Point out each Plasmodium parasite.
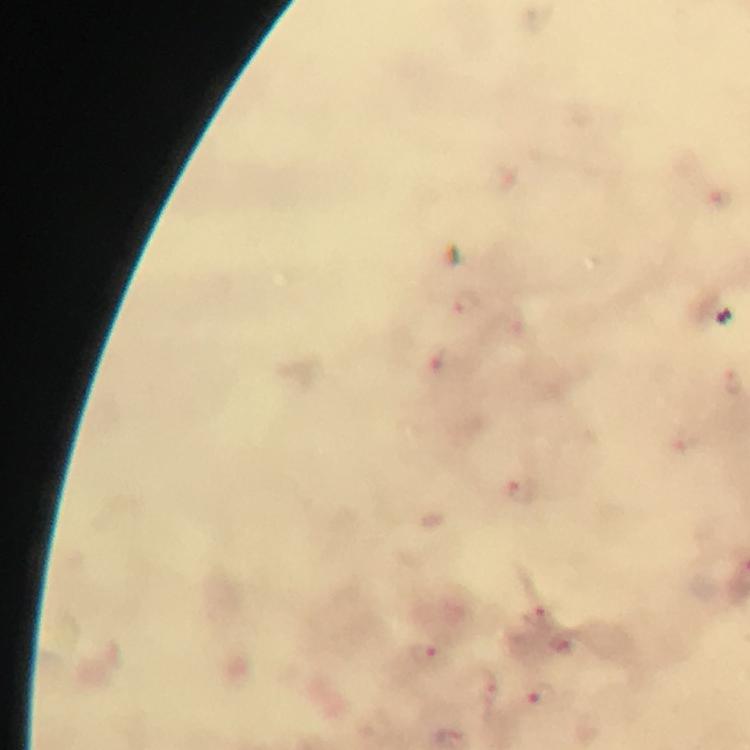
Approximate centers as {x, y} in pixels.
Plasmodium parasites: {721, 200}, {466, 302}, {435, 359}, {734, 383}, {519, 490}, {537, 616}, {564, 643}, {425, 655}, {487, 692}, {543, 694}.

Summary:
  - Stain: Giemsa
  - Image size: 750×750 pixels
  - Cropped from: one field of view
  - Magnification: 100x
  - Preparation: thick smear
  - Capture: smartphone mounted on the microscope
  - Immersion oil: used
  - Context: from a diagnostic examination for malaria